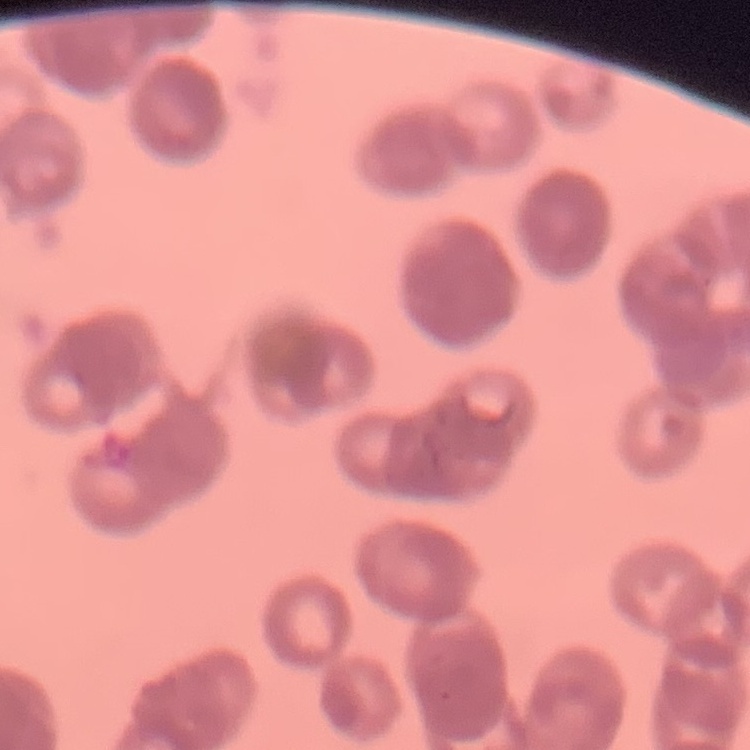

Summary:
  - Erythrocyte morphology: rouleaux formation
  - Image type: square crop of a larger photomicrograph
  - Stain: Field's or Giemsa
  - Preparation: thin peripheral smear